Comment on the morphology of the red blood cells.
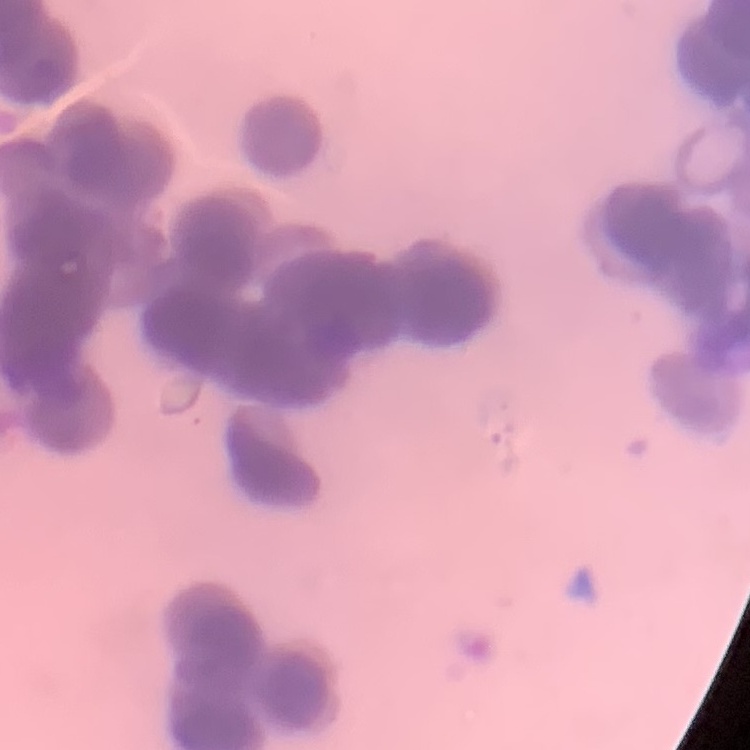

They show rouleaux formation.

Thin blood smear. One tile cut from a larger photomicrograph. Field's or Giemsa stain.